Identify the parasite.
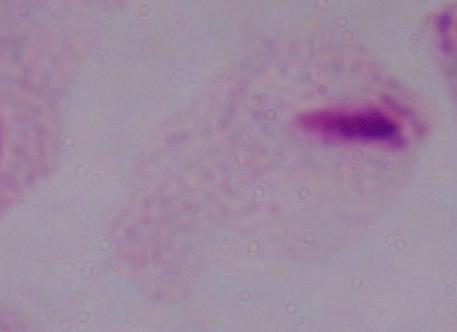

This is a trichomonad.

Captured at 1000x magnification. Micrograph.